State which parasite is depicted.
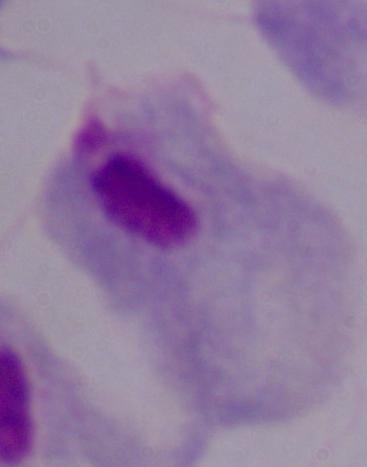

This is a trichomonad.

1000x magnification. Micrograph.